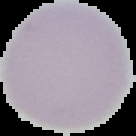
image size = 136×136 pixels
preparation = thin blood film
image type = segmented cell region on a black background
result = negative for Plasmodium parasites